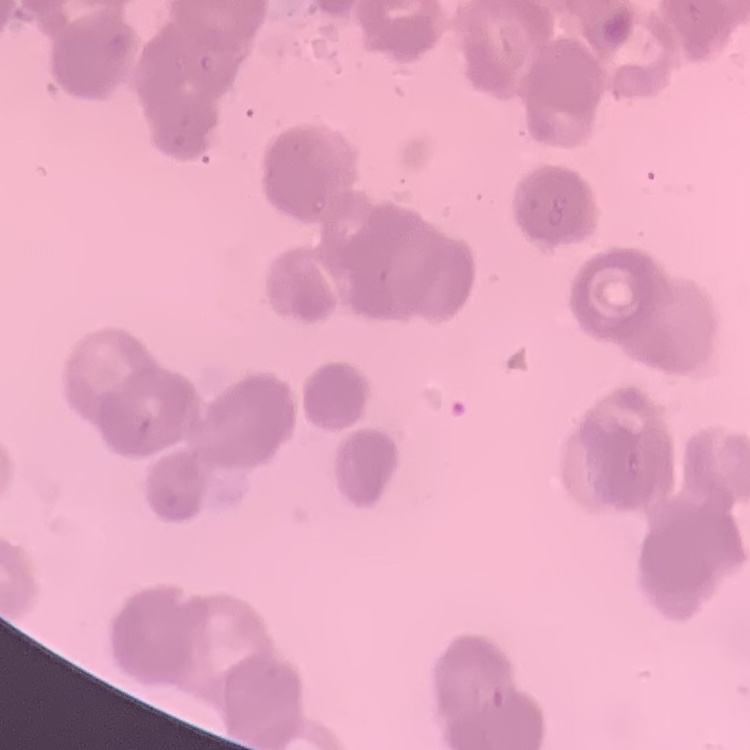

The red blood cells show rouleaux formation. Thin blood smear. Stained with either Field's or Giemsa. One tile cut from a larger photomicrograph.